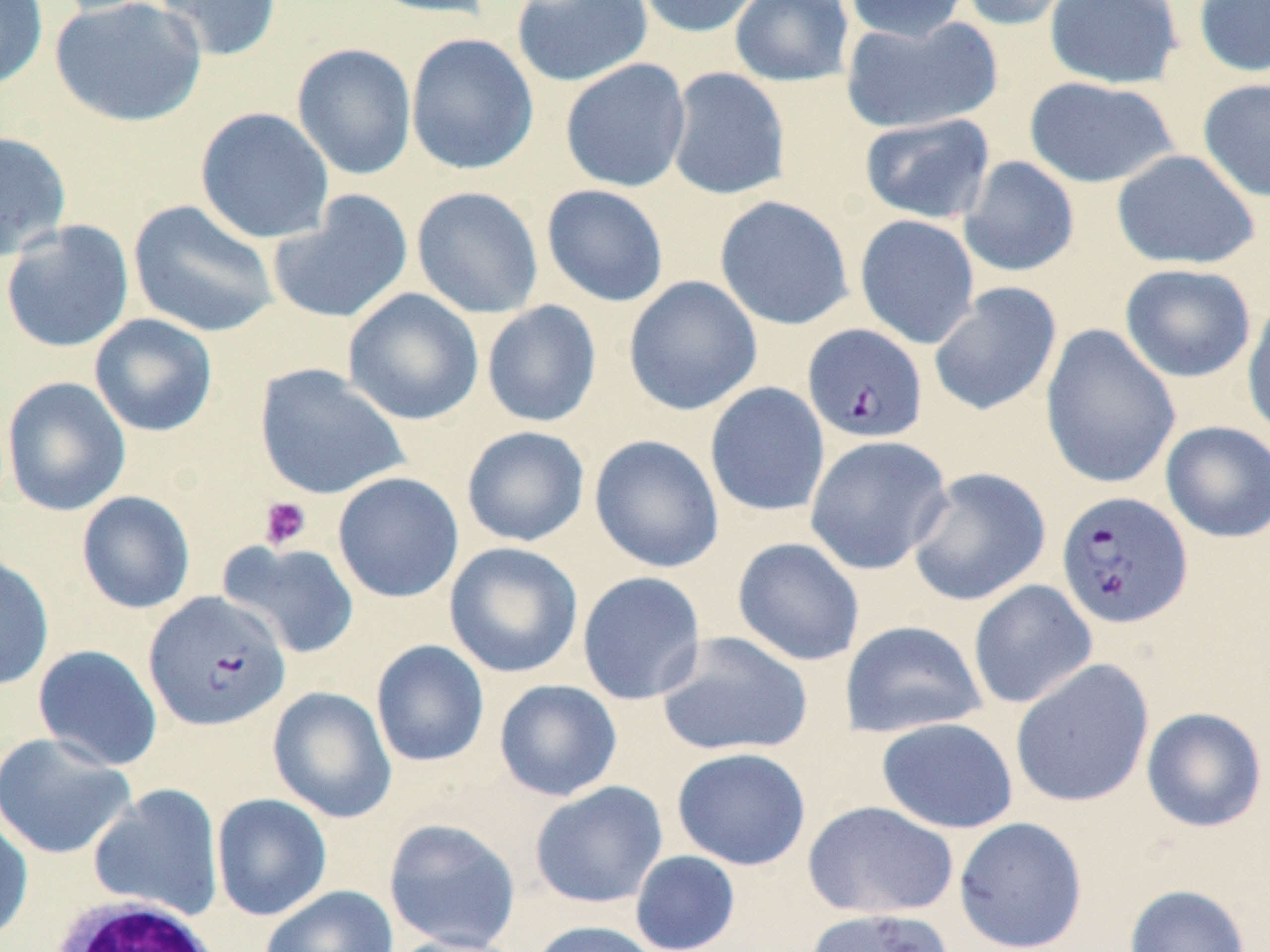 Approximate bounding boxes as (x1,y1)-(x2,y2) corner pairs in pixels. Platelet locations: (258,496)-(312,550). Plasmodium falciparum-infected red blood cell locations: (802,323)-(928,443), (1055,490)-(1193,630), (144,591)-(291,732). White blood cell locations: (43,893)-(227,952). Uninfected red blood cell locations: (0,0)-(48,93), (44,0)-(186,18), (49,0)-(208,127), (151,0)-(282,62), (359,0)-(502,20), (511,0)-(653,87), (634,0)-(767,38), (729,0)-(855,87), (842,0)-(972,43), (956,0)-(1083,32), (1044,0)-(1183,90), (1192,0)-(1270,78), (841,14)-(1001,135), (405,33)-(539,175), (292,43)-(417,181), (560,58)-(691,193), (666,67)-(790,200), (1023,76)-(1179,189), (1198,78)-(1270,203), (195,107)-(334,244), (858,112)-(996,224), (0,130)-(72,261), (1111,149)-(1260,270), (958,156)-(1080,278), (541,184)-(669,307), (411,186)-(544,318), (266,190)-(414,325), (714,195)-(854,330), (128,199)-(279,338), (854,214)-(980,349), (1,220)-(135,354), (1119,263)-(1256,383), (623,275)-(763,416), (928,282)-(1062,417), (342,288)-(485,426), (1241,296)-(1270,444), (481,300)-(602,428), (89,313)-(218,437), (1040,323)-(1181,491), (253,363)-(409,501), (1,376)-(131,517), (704,382)-(830,517), (1160,421)-(1270,543), (461,426)-(590,547), (588,434)-(724,573), (804,434)-(953,575), (906,466)-(1051,607), (332,472)-(464,603), (76,490)-(195,615), (732,537)-(865,667), (220,541)-(360,659), (443,542)-(584,679), (0,553)-(55,691), (576,571)-(706,705), (968,579)-(1097,709), (840,620)-(987,739), (654,631)-(814,758), (371,640)-(490,768), (32,644)-(163,771), (1010,658)-(1155,808), (494,679)-(622,802), (267,685)-(397,823), (1140,707)-(1268,833), (876,716)-(1018,833), (0,732)-(136,860), (671,747)-(812,871), (529,780)-(667,908), (88,784)-(224,920), (211,793)-(332,921), (802,800)-(959,920), (0,812)-(34,944), (953,816)-(1087,952), (383,817)-(521,952), (630,850)-(741,952), (1124,884)-(1250,952), (260,885)-(398,952), (801,906)-(955,952), (528,920)-(665,952), (383,933)-(527,952). Slide-level diagnosis: Plasmodium falciparum. Captured at 1000x magnification. Optical microscopy. Image is 1270×952 pixels. May-Grünwald-Giemsa-stained preparation. Thin blood smear. Single field of view.